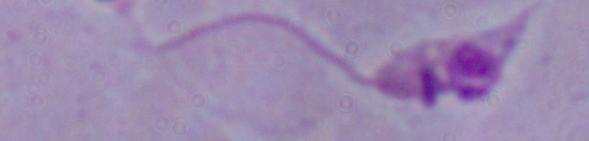
{
  "magnification": "1000x",
  "modality": "photomicrograph",
  "identification": "Leishmania"
}